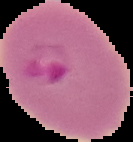
image type = segmented cell region with the area outside set to black
preparation = thin blood film
image size = 133×142 pixels
malaria status = parasitized